State which cell type is depicted.
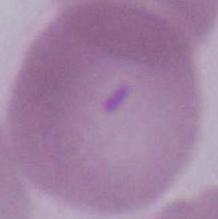

An erythrocyte.

Summary:
  - Magnification: 1000x
  - Modality: photomicrograph